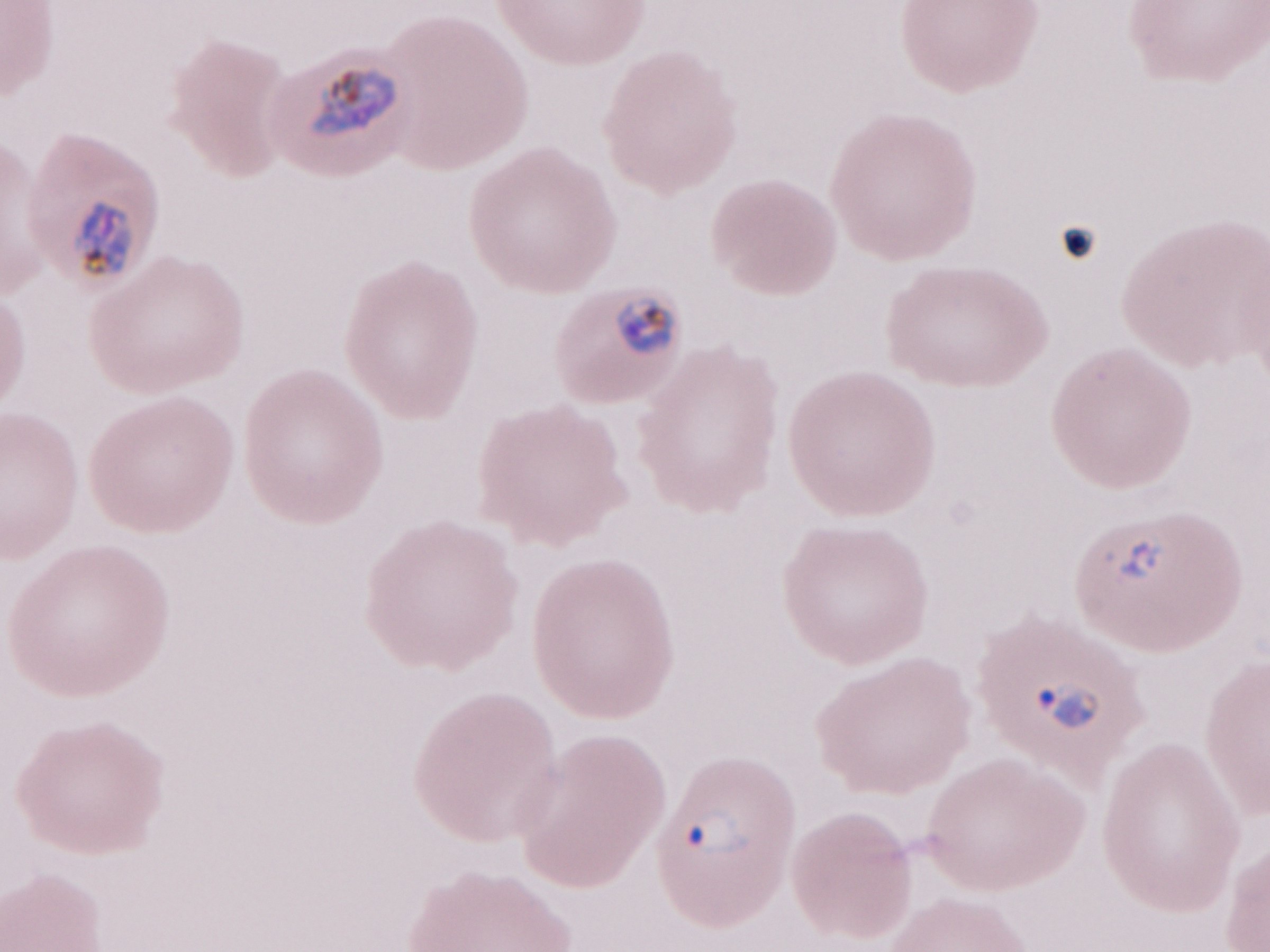 One field of this slide. Magnification: 1,000x. May-Grünwald-Giemsa stain. Image is 1270×952 pixels. Patient diagnosis: malaria infection. Thin blood film. Olympus BX43 microscope, Olympus DP73 camera.